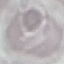
result = negative for malaria parasites
capture = smartphone camera at the microscope eyepiece
preparation = thin smear
image type = cell patch, automatically extracted from a larger field of view and resized to 64 × 64 pixels
stain = Giemsa